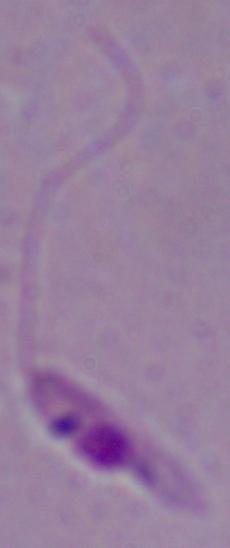

{
  "magnification": "1000x",
  "identification": "Leishmania",
  "modality": "micrograph"
}